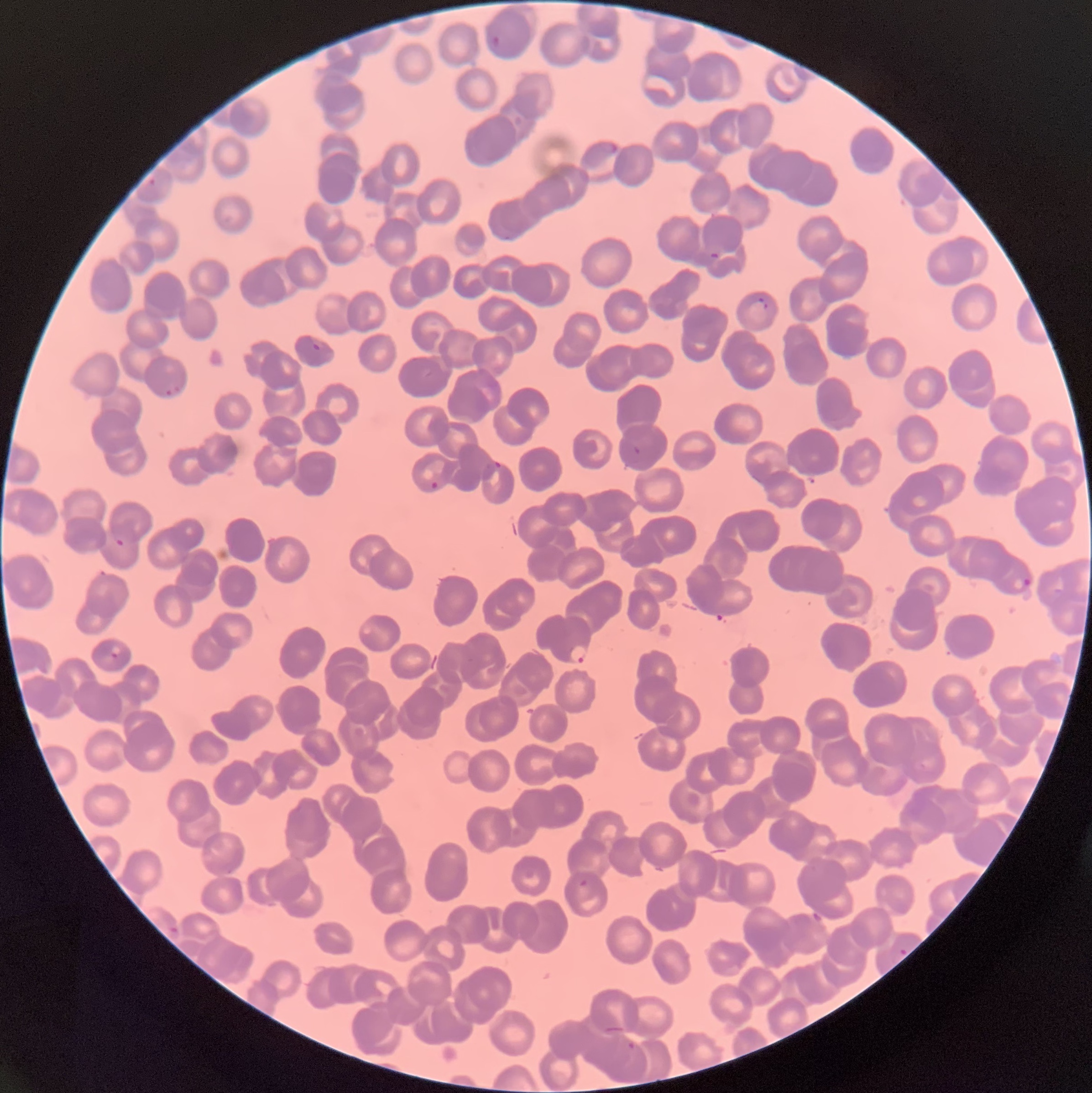

Approximate bounding boxes as named x1/y1/x2/y2 corners in pixels. Plasmodium parasite locations: (x1=492, y1=35, x2=501, y2=47), (x1=598, y1=140, x2=619, y2=155), (x1=146, y1=178, x2=157, y2=186), (x1=502, y1=236, x2=513, y2=242), (x1=708, y1=253, x2=720, y2=259), (x1=756, y1=297, x2=770, y2=311), (x1=312, y1=339, x2=325, y2=350), (x1=165, y1=386, x2=181, y2=395), (x1=632, y1=445, x2=641, y2=455), (x1=494, y1=461, x2=502, y2=468), (x1=430, y1=482, x2=439, y2=489), (x1=116, y1=537, x2=124, y2=546), (x1=1021, y1=578, x2=1031, y2=586), (x1=569, y1=646, x2=589, y2=664), (x1=110, y1=652, x2=119, y2=659), (x1=577, y1=879, x2=589, y2=887), (x1=168, y1=926, x2=179, y2=934), (x1=899, y1=949, x2=908, y2=955). The red blood cells show rouleaux formation. Light microscopy. Thin blood film. Image is 1092×1093 pixels.